State which parasite is depicted.
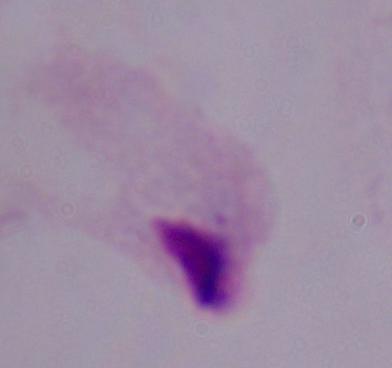

A trichomonad.

Summary:
  - Modality: photomicrograph
  - Magnification: 1000x